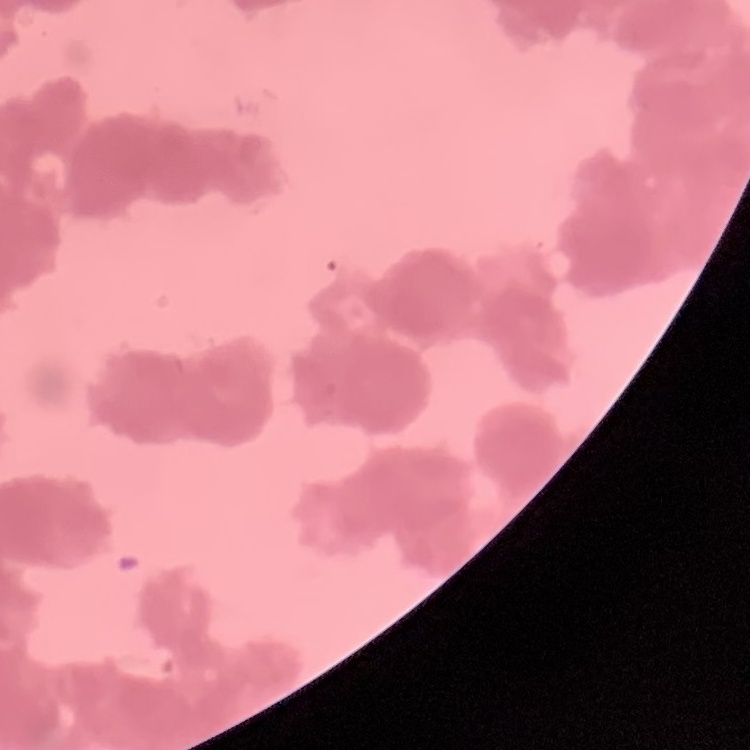
Summary:
  - Erythrocyte morphology: rouleaux formation
  - Stain: Field's or Giemsa
  - Preparation: thin peripheral smear
  - Image type: square crop of a larger photomicrograph